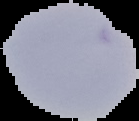
Malaria status: uninfected. The area outside the segmented cell region is set to black. Image is 139×121 pixels. From a thin blood smear.